Locate every Plasmodium parasite.
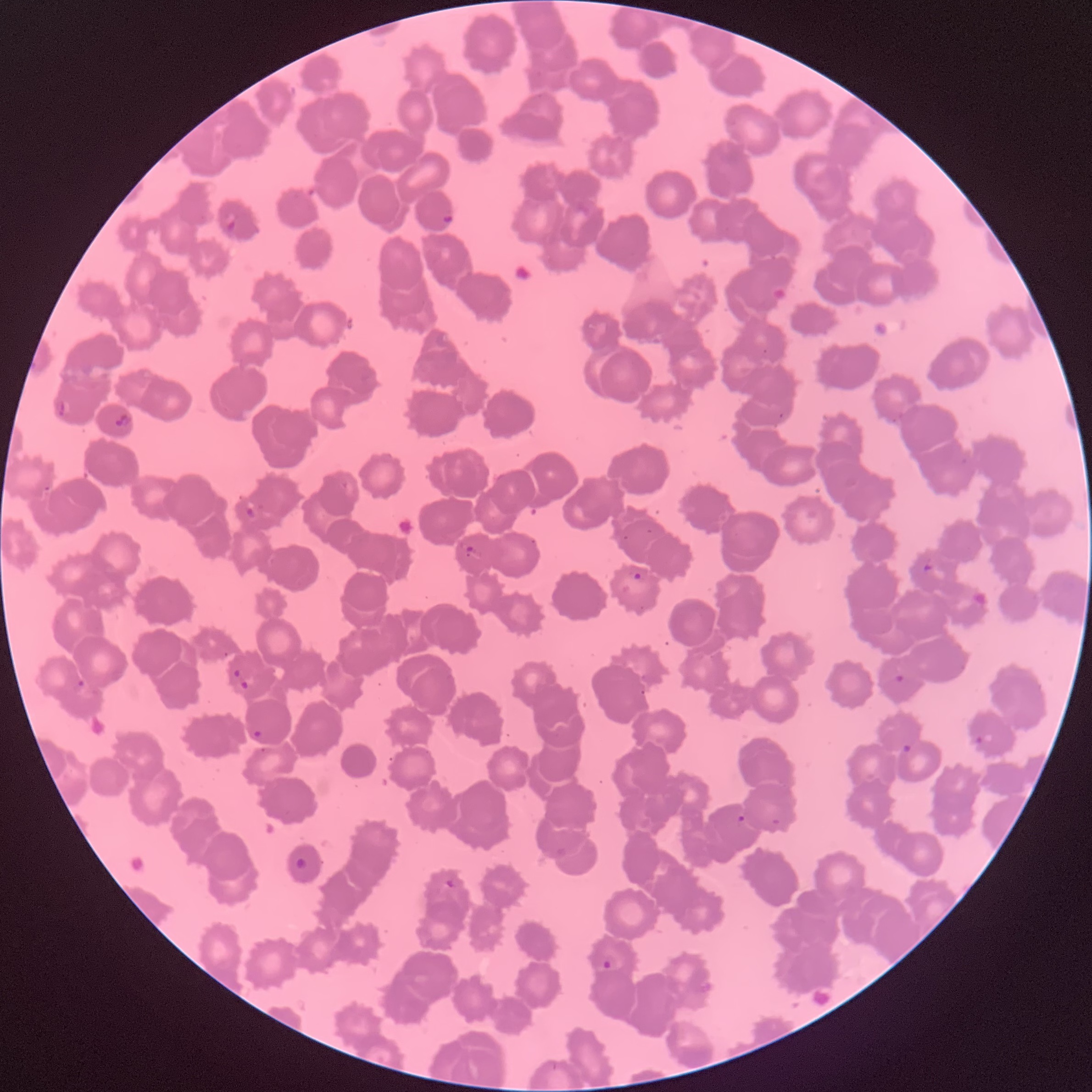

Approximate bounding boxes as [x1, y1, x2, y2] in pixels.
Plasmodium parasites: [225, 211, 238, 231], [441, 215, 455, 224], [58, 400, 67, 419], [115, 413, 133, 427], [245, 506, 256, 519], [464, 544, 479, 560], [922, 562, 933, 573], [632, 572, 643, 581], [233, 669, 241, 678], [894, 674, 905, 684], [76, 680, 86, 688], [239, 681, 249, 689], [252, 730, 263, 738], [975, 734, 984, 744], [902, 744, 913, 753], [736, 814, 746, 823], [294, 857, 308, 871], [443, 878, 456, 889], [602, 959, 613, 971].

Summary:
  - Red blood cell morphology: rouleaux formation
  - Preparation: thin blood smear
  - Image size: 1092×1092 pixels
  - Modality: light microscopy